Locate every blood parasite and identify its species.
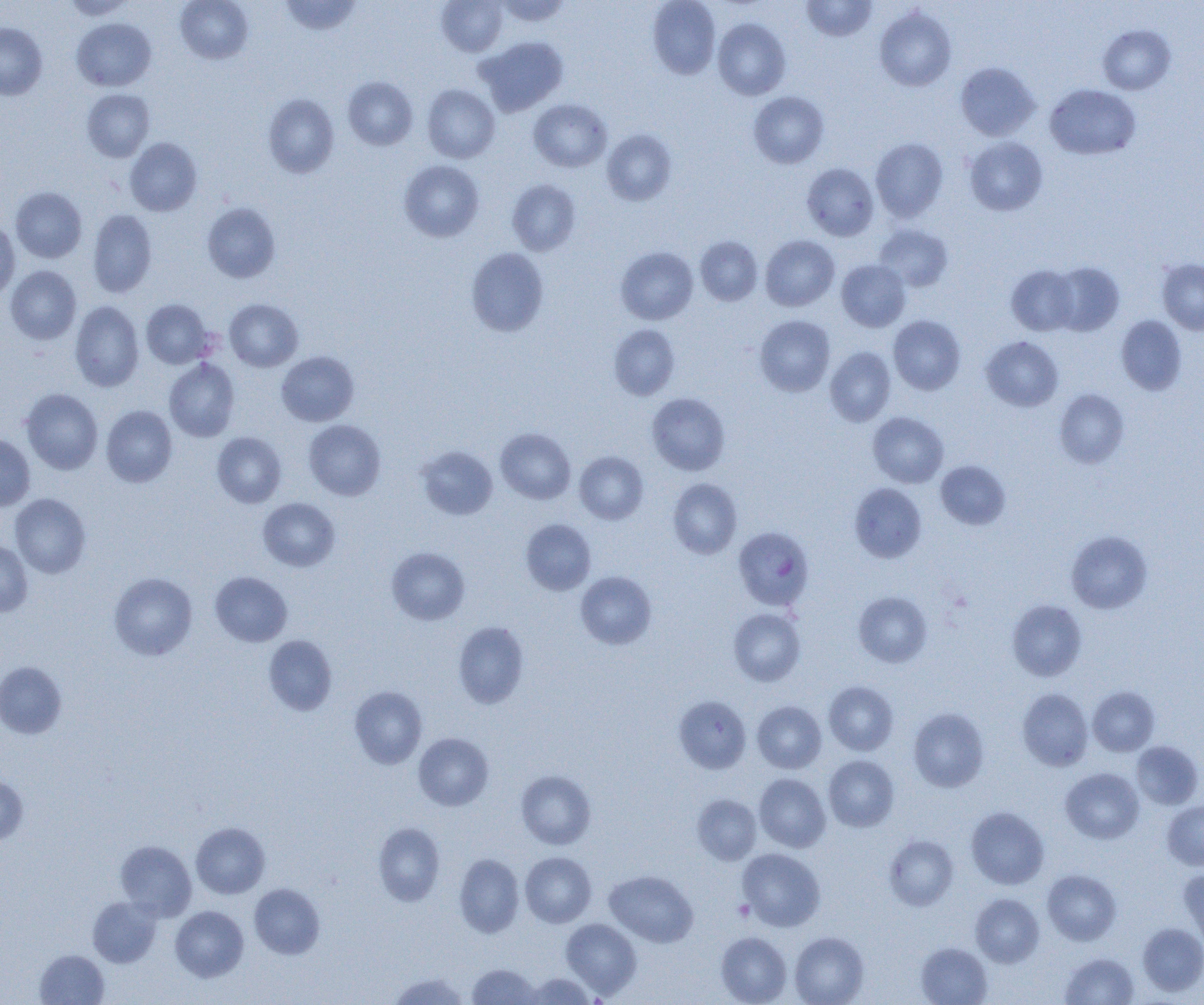
Approximate bounding boxes as [x1, y1, x2, y2] in pixels.
Plasmodium falciparum-infected red blood cells: [733, 526, 814, 611].
No Plasmodium ovale, Plasmodium malariae, Plasmodium vivax, Babesia divergens, or Trypanosoma brucei observed.

Uninfected red blood cell locations: [62, 0, 136, 20], [176, 0, 253, 64], [280, 0, 362, 35], [437, 0, 508, 56], [495, 0, 571, 25], [648, 0, 720, 79], [801, 0, 877, 42], [875, 7, 956, 91], [71, 18, 156, 91], [713, 18, 791, 100], [0, 22, 47, 100], [1097, 25, 1176, 95], [475, 36, 568, 116], [955, 62, 1041, 141], [343, 76, 417, 150], [422, 84, 500, 163], [1045, 84, 1141, 160], [82, 88, 154, 162], [748, 91, 829, 168], [263, 94, 339, 178], [529, 98, 612, 172], [602, 129, 677, 206], [125, 137, 202, 216], [870, 137, 949, 222], [965, 137, 1047, 216], [399, 160, 484, 242], [802, 163, 879, 241], [507, 179, 581, 256], [10, 187, 87, 263], [202, 202, 281, 283], [88, 210, 157, 297], [0, 219, 20, 301], [875, 224, 954, 292], [760, 235, 839, 311], [695, 236, 762, 305], [616, 246, 698, 324], [466, 247, 549, 337], [1157, 258, 1204, 335], [836, 259, 910, 331], [1049, 261, 1124, 336], [5, 265, 81, 345], [1007, 265, 1081, 335], [224, 298, 303, 371], [141, 299, 213, 368], [70, 301, 144, 392], [755, 315, 835, 396], [889, 315, 966, 395], [1116, 315, 1187, 395], [609, 324, 680, 400], [981, 335, 1063, 412], [825, 346, 896, 426], [276, 351, 359, 426], [164, 359, 239, 442], [21, 388, 103, 474], [1054, 389, 1129, 468], [647, 392, 730, 475], [101, 405, 177, 487], [868, 411, 948, 488], [304, 419, 386, 500], [495, 428, 575, 504], [212, 432, 286, 508], [0, 434, 35, 511], [417, 445, 498, 520], [574, 451, 649, 524], [935, 460, 1011, 530], [668, 478, 742, 558], [849, 483, 927, 563], [9, 493, 91, 578], [258, 497, 339, 571], [521, 519, 596, 595], [1066, 530, 1152, 614], [0, 540, 33, 617], [386, 547, 470, 625], [210, 571, 292, 646], [576, 571, 657, 649], [109, 572, 198, 660], [853, 591, 933, 668], [1007, 599, 1087, 681], [728, 608, 806, 686], [453, 621, 529, 708], [264, 635, 337, 715], [0, 661, 67, 738], [824, 680, 898, 755], [350, 686, 428, 768], [1087, 686, 1159, 756], [1017, 689, 1093, 771], [674, 695, 751, 774], [752, 700, 826, 773], [908, 708, 989, 792], [413, 733, 494, 810], [1131, 741, 1203, 809], [823, 755, 899, 831], [1060, 768, 1144, 844], [516, 770, 596, 849], [754, 773, 831, 852], [0, 774, 29, 845], [693, 794, 761, 865], [1163, 801, 1204, 870], [966, 806, 1049, 889], [191, 822, 270, 898], [373, 822, 445, 906], [884, 835, 959, 911], [115, 840, 197, 920], [738, 848, 825, 931], [520, 852, 596, 927], [454, 853, 524, 938], [1178, 867, 1204, 951], [1042, 869, 1121, 945], [605, 870, 698, 947], [249, 883, 325, 959], [970, 893, 1044, 968], [87, 896, 162, 968], [170, 906, 249, 982], [560, 918, 642, 998], [1138, 923, 1204, 996], [715, 931, 791, 1005], [789, 932, 869, 1005], [915, 942, 992, 1005], [35, 949, 109, 1005], [1059, 952, 1139, 1005], [467, 964, 539, 1004], [390, 972, 469, 1005], [523, 973, 595, 1004]. Platelet locations: [733, 900, 754, 921]. Slide-level diagnosis: Plasmodium falciparum. One field of a larger specimen. Optical microscopy. 1000x magnification. Thin blood smear. Image is 1204×1005 pixels.